Describe the morphology of the erythrocytes.
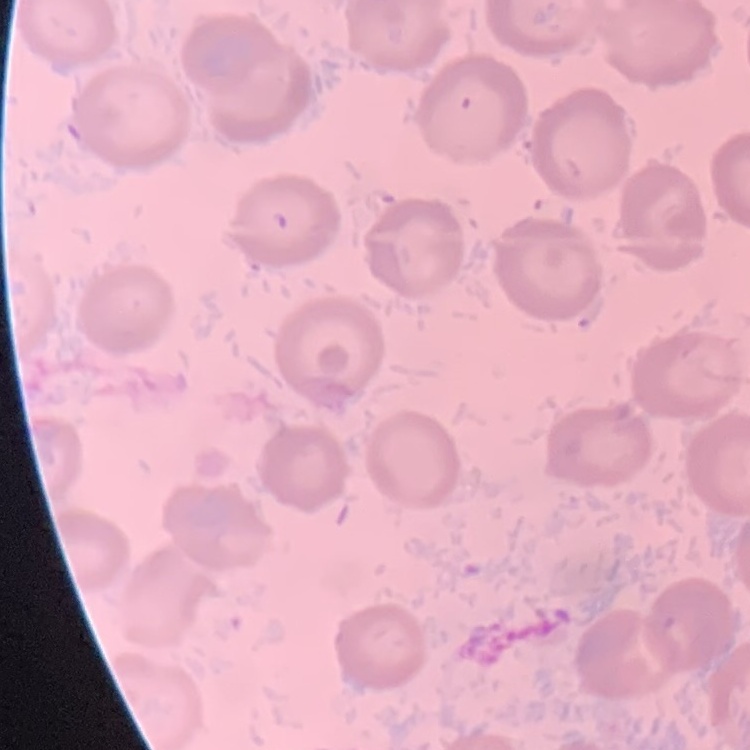

No rouleaux formation.

Square crop of a larger photomicrograph. Thin blood smear. Stained with either Field's or Giemsa.